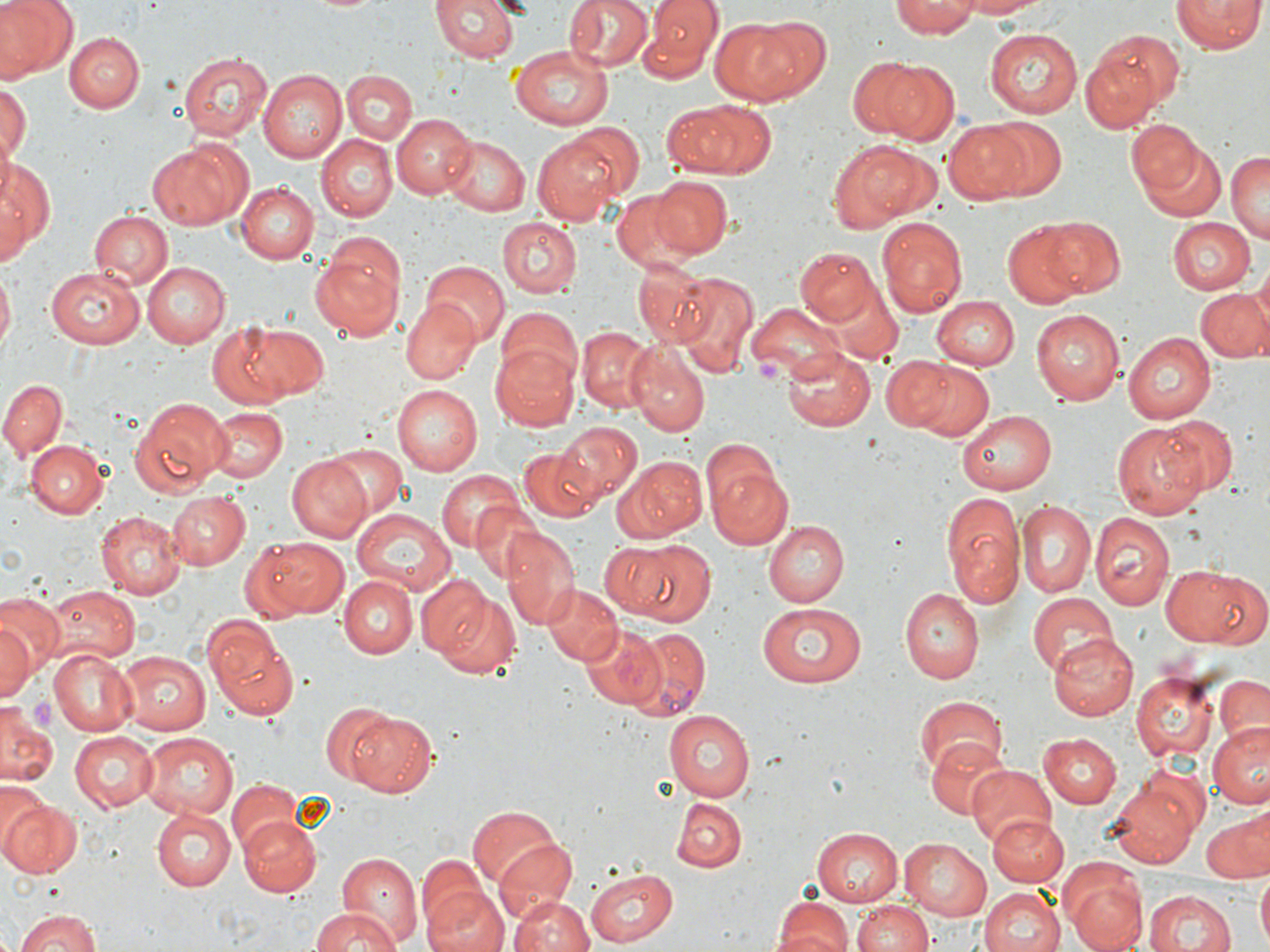

{
  "slide_level_diagnosis": "Plasmodium vivax",
  "preparation": "thin blood film",
  "platelet_locations": "approximate bounding boxes as (x1, y1, x2, y2) in pixels: (757, 357, 783, 384), (33, 699, 58, 735)",
  "plasmodium_vivax_infected_red_blood_cell_locations": "approximate bounding boxes as (x1, y1, x2, y2) in pixels: (623, 627, 710, 720)",
  "field_of_view": "single",
  "magnification": "1000x",
  "image_size": "1270×952 pixels",
  "uninfected_red_blood_cell_locations": "approximate bounding boxes as (x1, y1, x2, y2) in pixels: (1, 0, 76, 81), (429, 0, 520, 64), (565, 0, 653, 73), (646, 0, 721, 71), (893, 0, 980, 40), (957, 0, 1054, 18), (1172, 0, 1262, 55), (707, 16, 812, 107), (1092, 26, 1187, 116), (984, 27, 1080, 119), (64, 31, 143, 112), (512, 44, 615, 130), (1079, 48, 1163, 133), (178, 51, 273, 142), (851, 57, 957, 144), (262, 70, 349, 163), (340, 70, 414, 142), (1, 81, 28, 172), (674, 99, 775, 177), (1126, 112, 1212, 201), (391, 113, 477, 197), (980, 119, 1066, 198), (943, 120, 1038, 204), (532, 134, 625, 227), (314, 136, 396, 221), (1137, 137, 1229, 224), (441, 138, 530, 217), (830, 139, 931, 230), (147, 141, 248, 232), (1228, 151, 1269, 243), (0, 159, 54, 257), (647, 175, 734, 258), (236, 183, 318, 264), (0, 184, 28, 269), (610, 190, 700, 272), (89, 211, 173, 289), (496, 217, 581, 299), (878, 218, 968, 316), (1040, 218, 1124, 296), (1168, 218, 1255, 295), (1002, 221, 1088, 306), (795, 247, 878, 325), (309, 248, 404, 339), (1250, 259, 1270, 343), (420, 260, 509, 346), (143, 263, 229, 347), (633, 263, 714, 345), (45, 266, 145, 348), (0, 273, 14, 354), (676, 273, 758, 377), (829, 283, 904, 363), (1193, 286, 1268, 363), (931, 295, 1018, 369), (400, 297, 482, 386), (746, 302, 849, 383), (496, 307, 583, 387), (1031, 308, 1126, 405), (207, 322, 319, 408), (576, 327, 658, 413), (1122, 332, 1218, 422), (489, 342, 580, 431), (630, 344, 709, 435), (781, 345, 874, 431), (879, 357, 954, 432), (908, 360, 993, 440), (1, 378, 66, 464), (391, 385, 483, 474), (129, 396, 232, 496), (205, 406, 286, 483), (959, 409, 1057, 493), (1156, 415, 1239, 498), (1113, 420, 1207, 519), (557, 421, 639, 506), (28, 442, 108, 518), (330, 443, 406, 516), (518, 446, 602, 523), (616, 454, 707, 542), (284, 455, 373, 543), (707, 461, 796, 551), (437, 469, 526, 554), (938, 488, 1024, 610), (168, 491, 250, 569), (1017, 499, 1096, 601), (352, 509, 456, 596), (1089, 511, 1176, 612), (95, 513, 186, 598), (763, 518, 846, 608), (499, 526, 578, 629), (240, 534, 352, 621), (625, 542, 716, 624), (598, 546, 672, 617), (1161, 565, 1265, 650), (414, 574, 493, 659), (340, 577, 417, 658), (540, 583, 621, 666), (40, 585, 140, 665), (900, 588, 984, 682), (433, 590, 523, 678), (0, 592, 65, 670), (1027, 592, 1117, 675), (758, 601, 867, 690), (0, 614, 41, 704), (203, 616, 298, 720), (581, 624, 667, 710), (1049, 631, 1139, 720), (46, 647, 137, 737), (117, 650, 211, 735), (1132, 673, 1215, 761), (1213, 674, 1270, 746), (916, 694, 1008, 779), (320, 703, 399, 785), (0, 705, 61, 787), (343, 709, 438, 798), (663, 710, 753, 800), (1208, 721, 1269, 806), (70, 730, 159, 810), (1040, 731, 1123, 808), (138, 733, 237, 817), (929, 739, 1012, 822), (968, 765, 1056, 845), (226, 782, 302, 857), (1, 783, 48, 860), (1106, 784, 1196, 868), (0, 798, 80, 878), (672, 798, 746, 873), (154, 806, 238, 891), (469, 807, 562, 893), (1201, 812, 1270, 881), (237, 814, 321, 896), (989, 815, 1068, 887), (814, 828, 907, 907), (900, 837, 993, 919), (490, 839, 579, 928), (337, 852, 423, 946), (415, 857, 491, 939), (585, 867, 677, 946), (1256, 871, 1270, 949), (1064, 872, 1148, 952), (421, 882, 512, 952), (980, 887, 1065, 952), (1145, 890, 1236, 952), (508, 895, 594, 952), (773, 897, 853, 952), (853, 900, 936, 952), (308, 907, 402, 952), (14, 909, 101, 952)",
  "modality": "light microscopy",
  "stain": "May-Grünwald-Giemsa"
}